Classify this cell by malaria status.
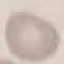
Uninfected.

Thin blood film. Photographed with a smartphone camera at the microscope eyepiece. Cell patch, automatically extracted from a larger field of view and resized to 64 × 64 pixels. Giemsa-stained preparation.